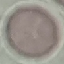
Summary:
  - Result: no malaria parasites seen
  - Preparation: thin smear
  - Image type: automatically extracted cell patch, resized to 64 × 64 pixels
  - Stain: Giemsa
  - Capture: smartphone through the microscope eyepiece